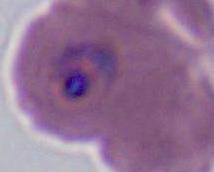
Summary:
  - Modality: photomicrograph
  - Magnification: 400x or 1000x
  - Identification: Plasmodium